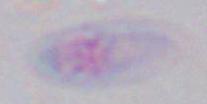
Summary:
  - Modality: micrograph
  - Magnification: 1000x
  - Identification: Toxoplasma gondii